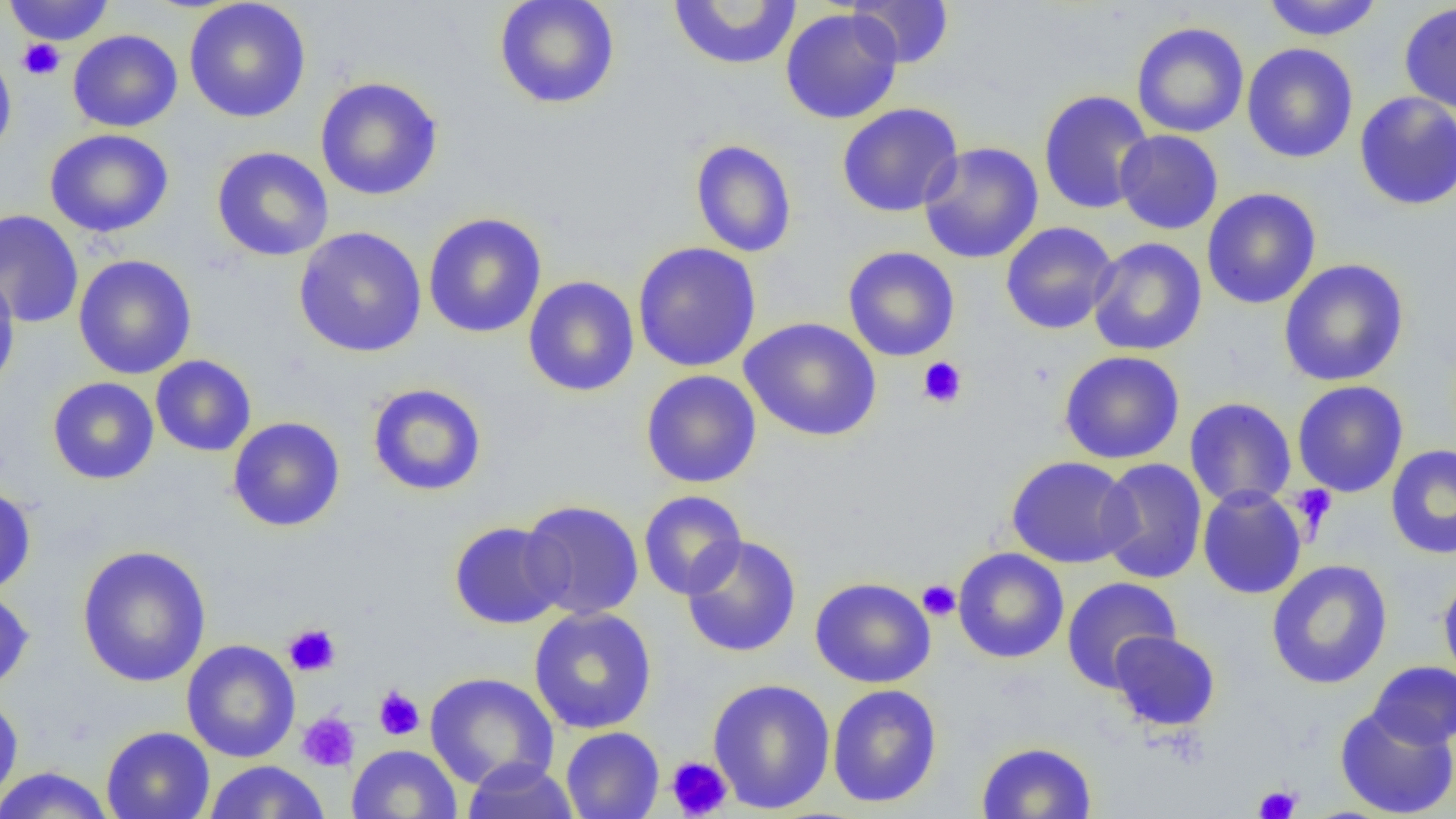
Summary:
  - Coordinate format: approximate bounding boxes as [x1, y1, x2, y2] in pixels
  - Uninfected red blood cell locations: [3, 0, 116, 46], [184, 0, 311, 123], [493, 0, 621, 110], [667, 0, 802, 71], [846, 0, 955, 69], [1260, 0, 1384, 41], [1398, 2, 1456, 113], [780, 8, 903, 124], [1131, 22, 1249, 139], [67, 29, 183, 132], [1242, 43, 1358, 163], [0, 50, 16, 161], [315, 76, 443, 201], [1039, 90, 1154, 215], [1354, 91, 1456, 211], [836, 103, 963, 218], [45, 128, 174, 238], [1114, 130, 1223, 234], [690, 139, 797, 258], [918, 141, 1044, 264], [211, 146, 334, 262], [1202, 188, 1321, 310], [0, 209, 84, 329], [422, 212, 547, 339], [1000, 221, 1118, 335], [293, 226, 428, 358], [1087, 237, 1207, 356], [632, 242, 762, 373], [843, 246, 960, 361], [73, 254, 197, 380], [1278, 259, 1409, 386], [0, 270, 20, 394], [523, 276, 640, 397], [739, 318, 882, 442], [1059, 350, 1185, 464], [150, 354, 257, 457], [640, 369, 761, 488], [47, 377, 159, 485], [1292, 380, 1409, 497], [367, 382, 487, 497], [1184, 398, 1297, 509], [227, 416, 346, 532], [1386, 444, 1456, 559], [1006, 455, 1137, 568], [1096, 457, 1208, 584], [0, 485, 36, 597], [1197, 485, 1307, 600], [638, 490, 747, 599], [519, 499, 644, 620], [448, 521, 568, 629], [680, 535, 802, 658], [76, 545, 211, 687], [953, 547, 1069, 664], [1266, 559, 1393, 690], [1438, 570, 1456, 689], [810, 576, 935, 688], [1061, 576, 1181, 692], [0, 586, 34, 695], [528, 606, 657, 734], [1108, 630, 1221, 731], [181, 639, 300, 763], [1368, 661, 1456, 750], [424, 672, 559, 790], [707, 678, 836, 814], [827, 684, 942, 808], [0, 691, 24, 810], [1334, 704, 1455, 818], [100, 726, 215, 819], [560, 727, 664, 819], [976, 741, 1097, 819], [346, 744, 462, 819], [461, 758, 580, 819], [201, 760, 330, 819], [0, 766, 116, 819]
  - Platelet locations: [17, 39, 65, 80], [917, 357, 967, 408], [1291, 484, 1337, 537], [917, 580, 961, 621], [282, 622, 341, 677], [374, 686, 425, 740], [297, 712, 360, 772], [665, 756, 733, 818], [1253, 784, 1301, 819]
  - Slide-level diagnosis: negative for blood parasites
  - Magnification: 1000x
  - Image size: 1456×819 pixels
  - Preparation: thin blood film
  - Field of view: single
  - Modality: optical microscopy